Identify the parasite.
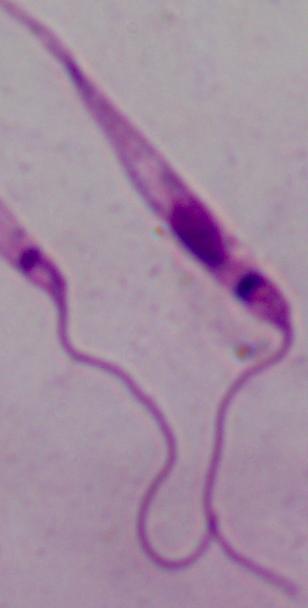
This is Leishmania.

Photomicrograph. Captured at 1000x magnification.